Name the blood parasite species.
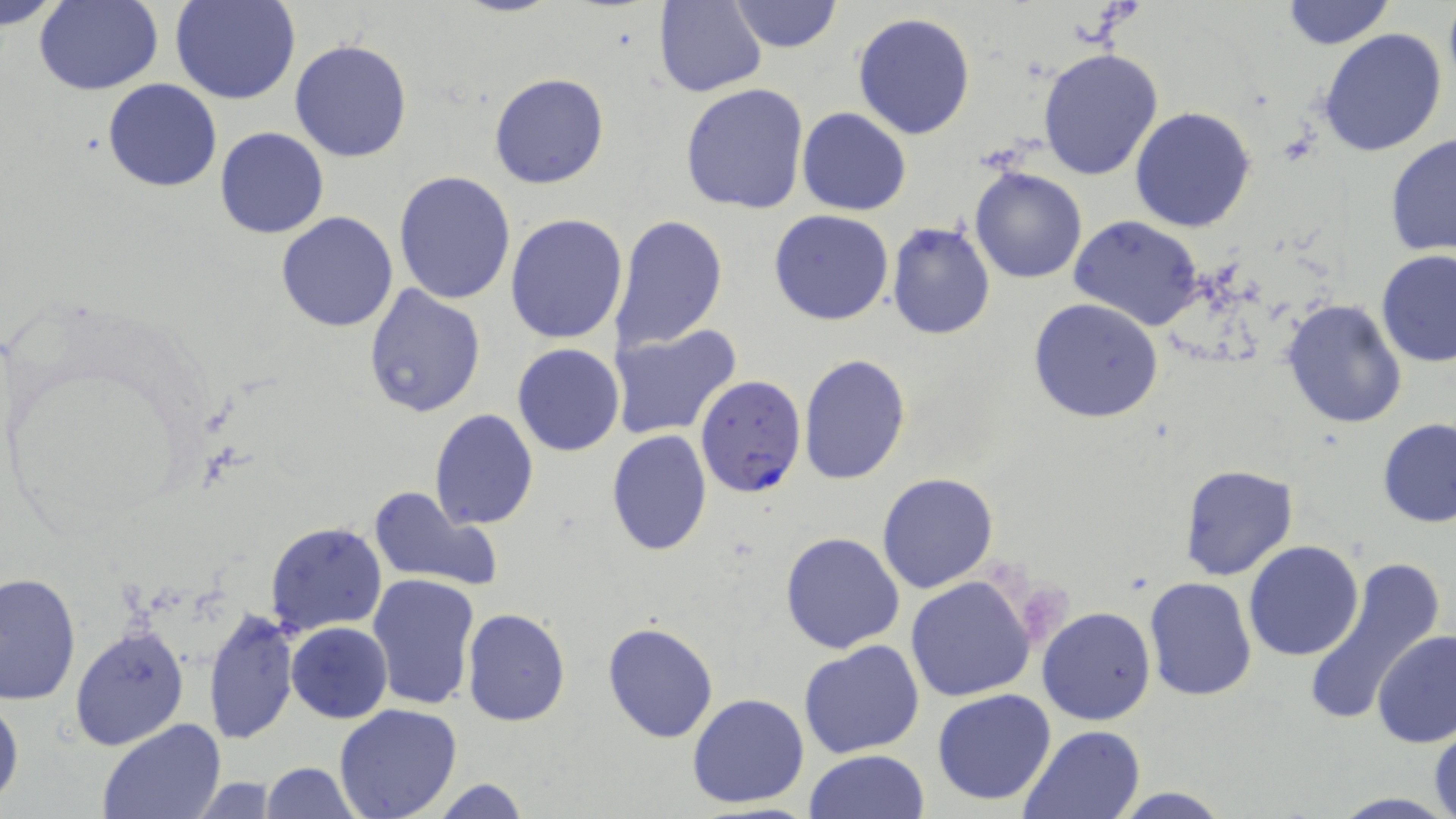
Plasmodium falciparum.

Approximate bounding boxes as [x1, y1, x2, y2] in pixels. Uninfected red blood cell locations: [1, 0, 67, 30], [171, 0, 300, 105], [725, 0, 844, 53], [1278, 0, 1397, 50], [1441, 0, 1456, 98], [34, 1, 164, 95], [654, 1, 767, 97], [852, 12, 978, 140], [1317, 28, 1448, 158], [289, 39, 412, 163], [1037, 46, 1165, 180], [488, 72, 610, 191], [103, 78, 222, 194], [680, 83, 810, 214], [1130, 106, 1256, 231], [797, 107, 911, 215], [214, 126, 329, 239], [1385, 131, 1456, 259], [970, 166, 1087, 283], [393, 170, 518, 304], [769, 210, 894, 326], [276, 211, 399, 332], [505, 213, 630, 344], [612, 214, 730, 352], [1069, 217, 1206, 330], [887, 220, 996, 340], [1375, 250, 1456, 368], [362, 284, 486, 417], [1028, 298, 1166, 424], [1281, 298, 1408, 431], [608, 324, 743, 440], [512, 343, 625, 457], [798, 353, 912, 486], [429, 409, 539, 530], [1377, 418, 1456, 528], [607, 429, 712, 557], [1178, 464, 1298, 581], [877, 471, 999, 593], [367, 484, 503, 594], [265, 521, 388, 638], [780, 532, 905, 654], [1244, 540, 1365, 660], [1298, 558, 1444, 717], [0, 571, 80, 706], [366, 574, 480, 710], [905, 574, 1037, 704], [1143, 575, 1256, 701], [1037, 605, 1156, 725], [203, 608, 299, 745], [462, 608, 571, 728], [287, 620, 393, 724], [602, 622, 719, 743], [70, 624, 191, 752], [1372, 630, 1456, 747], [800, 639, 925, 758], [932, 688, 1057, 808], [0, 692, 23, 808], [686, 693, 810, 810], [333, 704, 463, 819], [97, 718, 227, 819], [1429, 720, 1456, 819], [1018, 724, 1147, 819], [805, 749, 930, 819], [257, 762, 362, 818], [182, 777, 288, 815], [422, 778, 532, 819], [1105, 788, 1234, 819]. Plasmodium falciparum-infected red blood cell locations: [695, 375, 807, 499]. One field of a larger specimen. 1000x magnification. May-Grünwald-Giemsa-stained preparation. Light microscopy. Image is 1456×819 pixels. Thin blood smear.